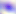

Toxoplasma gondii is shown. Micrograph. Captured at 400x magnification.